Assess this cell for malaria.
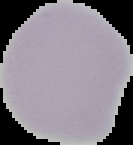

Uninfected.

Image is 133×145 pixels. The area outside the segmented cell region is set to black. From a thin blood film.